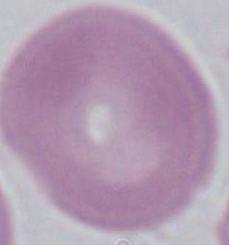 Captured at 1000x magnification. A red blood cell is shown. Photomicrograph.